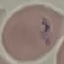
malaria status = parasitized
capture = smartphone camera at the microscope eyepiece
stain = Giemsa
image type = cell patch, automatically extracted from a larger field of view and resized to 64 × 64 pixels
preparation = thin blood smear